Name the parasite shown.
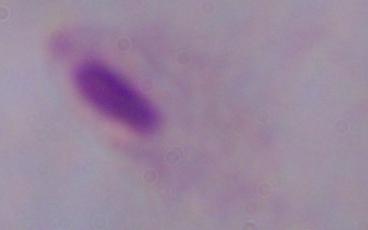
This is a trichomonad.

modality = photomicrograph
magnification = 1000x